Report the malaria status of this cell.
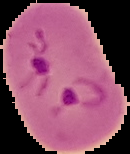

Parasitized.

Summary:
  - Preparation: thin blood smear
  - Image type: segmented cell region on a black background
  - Image size: 130×154 pixels